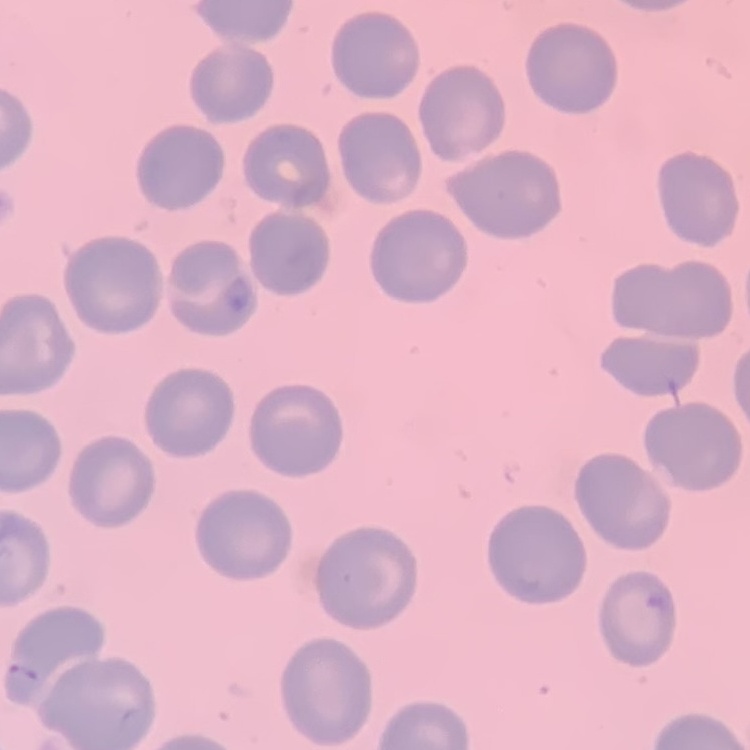
The red blood cells show no rouleaux formation. One tile cut from a larger photomicrograph. Thin peripheral smear. Stained with either Field's or Giemsa.